Name the parasite shown.
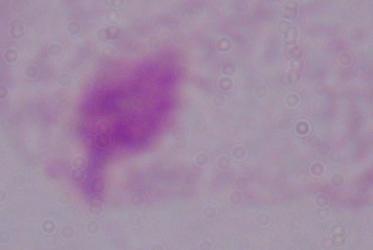

A trichomonad.

magnification = 1000x
modality = photomicrograph